Assess this cell for malaria.
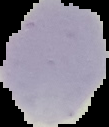
Uninfected.

Summary:
  - Image type: segmented cell region on a black background
  - Image size: 109×127 pixels
  - Preparation: thin blood film